Name the parasite shown.
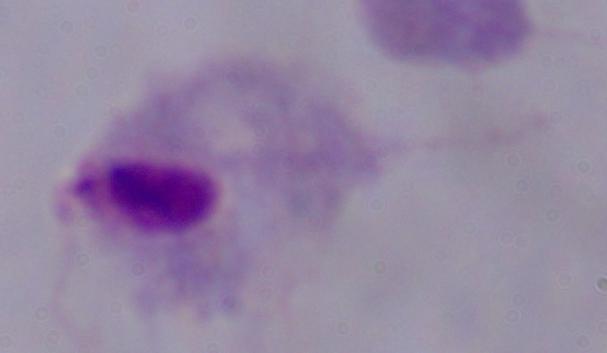

A trichomonad.

{
  "modality": "micrograph",
  "magnification": "1000x"
}